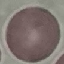 Malaria status: uninfected. Thin smear of blood. Photographed with a smartphone camera at the microscope eyepiece. Giemsa stain. Cell patch, automatically extracted from a larger field of view and resized to 64 × 64 pixels.